Classify the preparation.
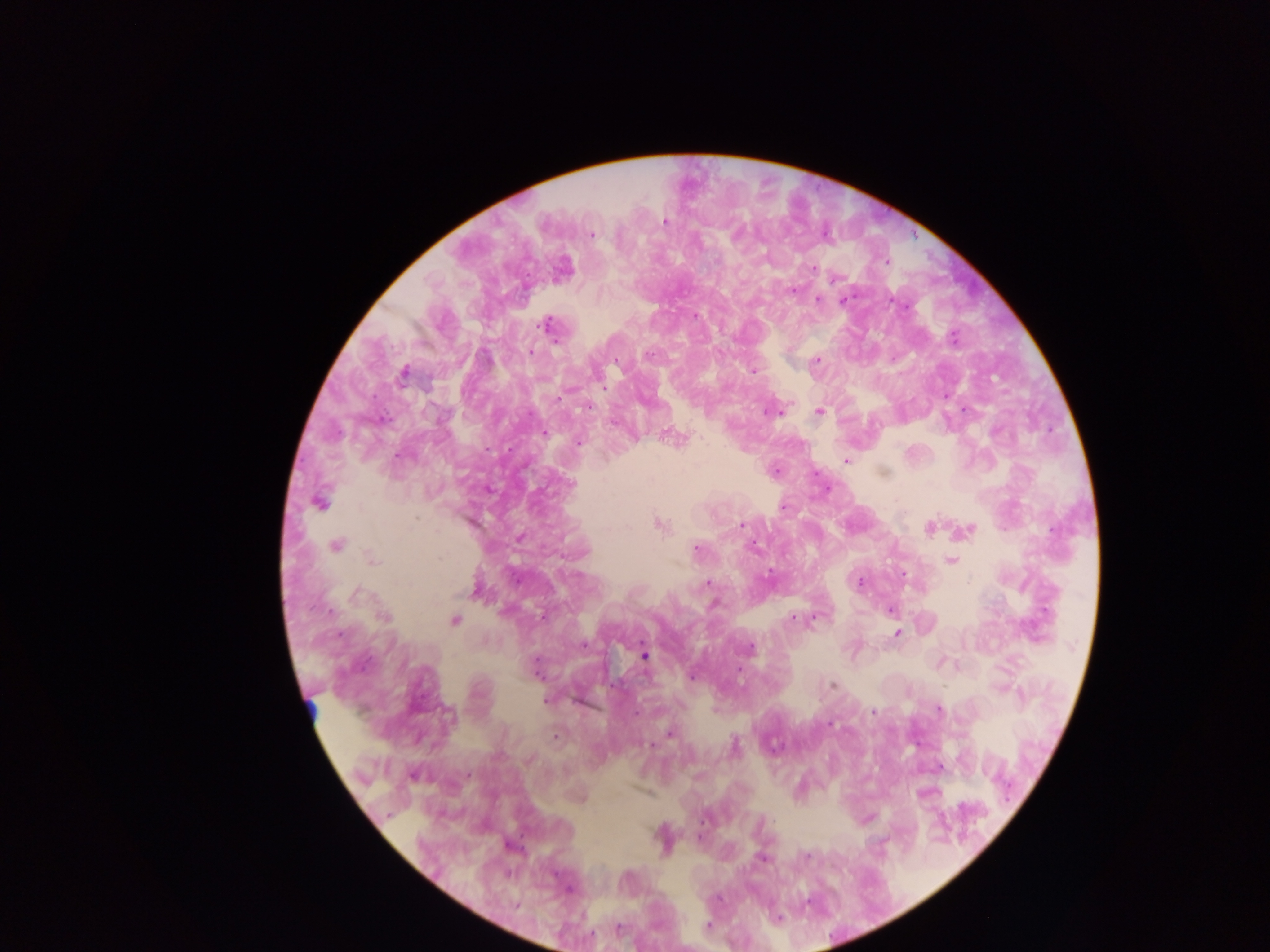
Thick blood smear.

Approximate centers as {x, y} in pixels. Plasmodium parasite locations: {665, 222}, {737, 234}, {592, 235}, {814, 268}, {835, 279}, {793, 291}, {818, 299}, {843, 301}, {695, 316}, {546, 326}, {954, 338}, {531, 353}, {648, 355}, {817, 360}, {753, 371}, {403, 374}, {557, 399}, {587, 407}, {819, 411}, {770, 412}, {543, 433}, {579, 442}, {846, 461}, {571, 484}, {319, 502}, {784, 507}, {658, 524}, {741, 524}, {930, 528}, {967, 530}, {336, 545}, {753, 548}, {696, 549}, {372, 560}, {950, 560}, {769, 574}, {860, 581}, {708, 583}, {475, 591}, {357, 594}, {714, 604}, {891, 610}, {385, 617}, {543, 618}, {793, 618}, {455, 620}, {897, 634}, {340, 635}, {584, 644}, {750, 647}, {644, 656}, {535, 667}, {740, 671}, {692, 677}, {833, 684}, {547, 700}, {939, 710}, {873, 712}, {829, 723}, {670, 734}, {556, 737}, {650, 745}, {735, 745}, {806, 857}, {762, 858}, {516, 905}, {708, 925}, {619, 928}. Leukocyte locations: {312, 708}. Image is 1270×952 pixels. Single field of view. Collected in Ghana. Photographed through a microscope with a mobile-phone camera.